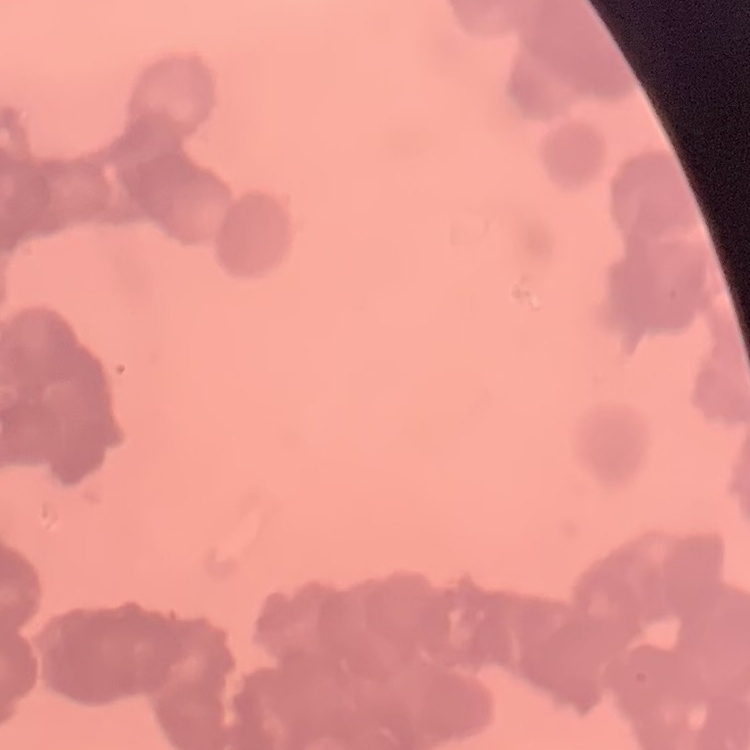

The erythrocytes exhibit rouleaux formation. Thin peripheral smear. One tile cut from a larger photomicrograph. Field's or Giemsa stain.